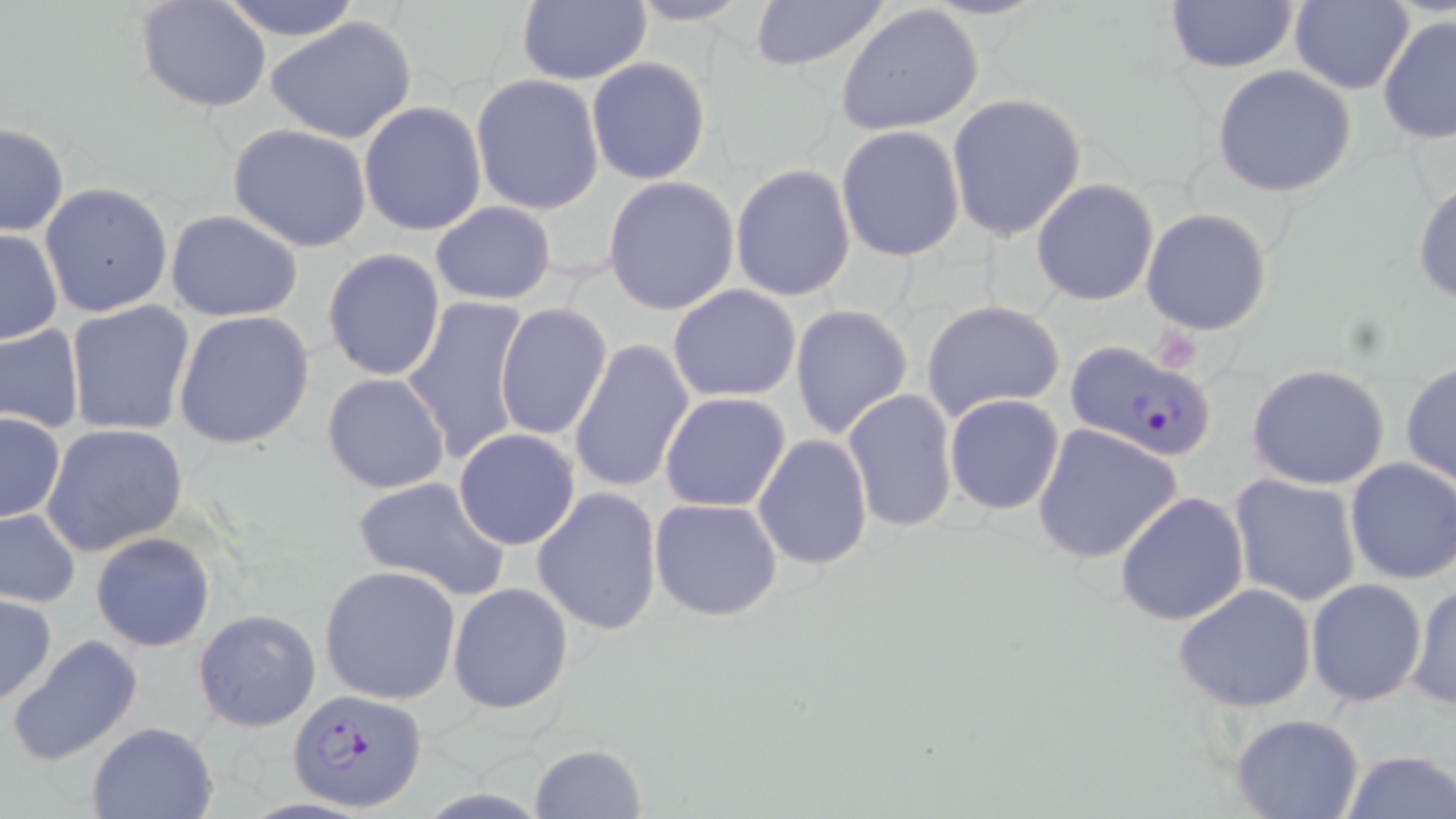

{
  "slide_level_diagnosis": "Plasmodium falciparum",
  "uninfected_red_blood_cell_locations": "approximate bounding boxes as (x1, y1, x2, y2) in pixels: (135, 0, 273, 112), (214, 0, 365, 41), (515, 0, 650, 87), (625, 0, 755, 26), (1162, 0, 1302, 73), (1291, 0, 1415, 95), (745, 1, 889, 73), (836, 4, 986, 138), (1378, 12, 1456, 145), (264, 15, 418, 145), (586, 56, 712, 186), (1211, 65, 1357, 197), (471, 74, 606, 215), (947, 93, 1087, 239), (358, 101, 488, 237), (0, 123, 69, 237), (228, 123, 374, 251), (836, 125, 966, 264), (730, 165, 858, 303), (602, 176, 740, 316), (1411, 178, 1456, 305), (1032, 179, 1160, 306), (40, 181, 173, 319), (429, 201, 556, 305), (1140, 208, 1275, 336), (166, 209, 303, 321), (1, 228, 63, 345), (322, 249, 446, 382), (667, 284, 803, 402), (401, 296, 533, 467), (920, 299, 1067, 424), (66, 301, 195, 437), (495, 303, 614, 439), (790, 305, 913, 439), (171, 311, 315, 450), (0, 324, 86, 434), (569, 340, 695, 495), (1400, 360, 1455, 488), (1246, 364, 1390, 490), (322, 372, 451, 493), (840, 389, 961, 533), (661, 391, 792, 512), (944, 394, 1066, 515), (1, 412, 66, 523), (41, 423, 189, 556), (1031, 423, 1182, 564), (453, 428, 581, 550), (752, 434, 872, 570), (1345, 457, 1456, 585), (1229, 473, 1363, 607), (351, 477, 511, 602), (532, 488, 663, 636), (1115, 490, 1250, 627), (649, 496, 783, 623), (0, 507, 80, 610), (91, 532, 216, 653), (319, 564, 461, 705), (1305, 579, 1428, 706), (1406, 582, 1456, 711), (447, 583, 573, 715), (1173, 584, 1318, 714), (0, 593, 57, 708), (193, 608, 322, 732), (7, 634, 143, 766), (1229, 713, 1365, 819), (86, 721, 221, 818), (530, 743, 648, 818), (1338, 748, 1455, 819)",
  "field_of_view": "one of a larger specimen",
  "modality": "optical microscopy",
  "preparation": "thin blood film",
  "image_size": "1456×819 pixels",
  "magnification": "1000x",
  "stain": "May-Grünwald-Giemsa",
  "plasmodium_falciparum_infected_red_blood_cell_locations": "approximate bounding boxes as (x1, y1, x2, y2) in pixels: (1066, 341, 1215, 463), (290, 689, 427, 811)"
}